Identify the parasite.
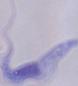
A trypanosome.

{
  "magnification": "1000x",
  "modality": "micrograph"
}